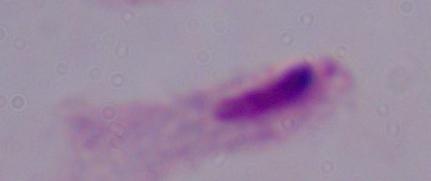 Photomicrograph. A trichomonad is seen. Captured at 1000x magnification.